State which parasite is depicted.
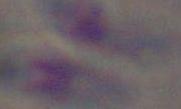
This is Toxoplasma gondii.

{
  "magnification": "1000x",
  "modality": "micrograph"
}